Name the parasite shown.
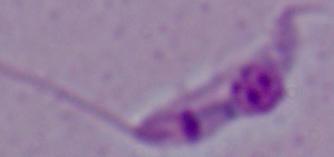
Leishmania.

Summary:
  - Modality: micrograph
  - Magnification: 1000x